Locate every P. falciparum parasite and identify its life-cycle stage.
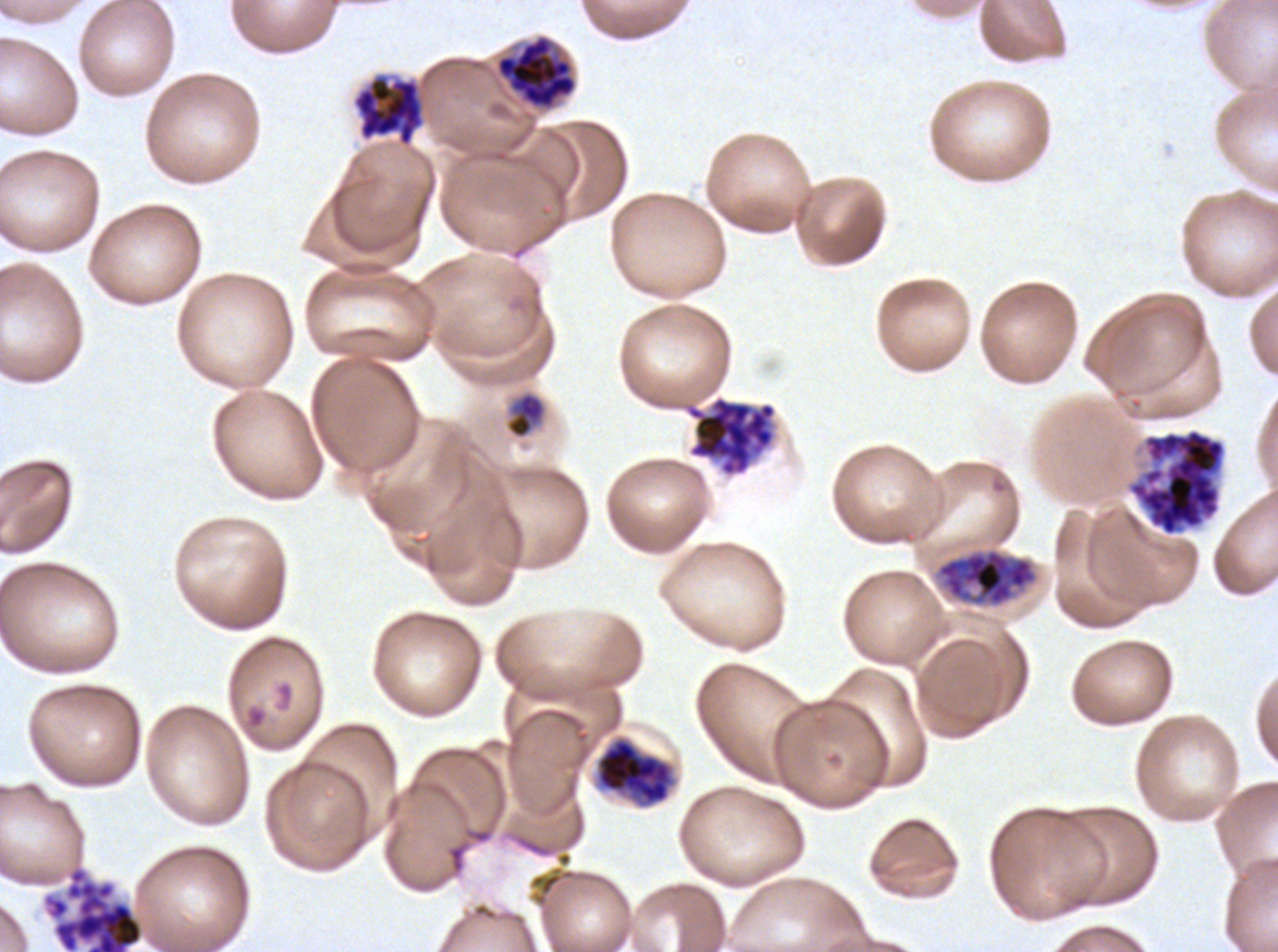

Approximate bounding boxes as [x1, y1, x2, y2] in pixels.
Late-ring/early-trophozoite forms: [506, 392, 546, 439].
Early schizonts: [935, 547, 1038, 607].
Late schizonts: [495, 34, 577, 111], [596, 737, 675, 807].
Segmenters: [352, 75, 424, 146], [685, 396, 777, 477], [1127, 428, 1226, 537], [41, 864, 144, 951].
No rings, mid trophozoites, late trophozoites, or gametocytes observed.

Image is 1278×952 pixels. Thin blood smear. Life-cycle stages observed: late-ring/early-trophozoite, early schizont, late schizont, segmenter. One sub-image of a larger composite. P. falciparum from a patient in The Gambia, cultured ex vivo for 24 to 48 hours. Giemsa-stained preparation.